Classify this cell by malaria status.
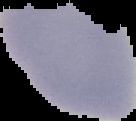

Uninfected.

From a thin blood smear. Image is 136×121 pixels. The area outside the segmented cell region is set to black.